Classify this cell by malaria status.
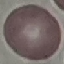
Uninfected.

{
  "image_type": "automatically extracted cell patch, resized to 64 × 64 pixels",
  "preparation": "thin blood smear",
  "capture": "smartphone through the microscope eyepiece",
  "stain": "Giemsa"
}